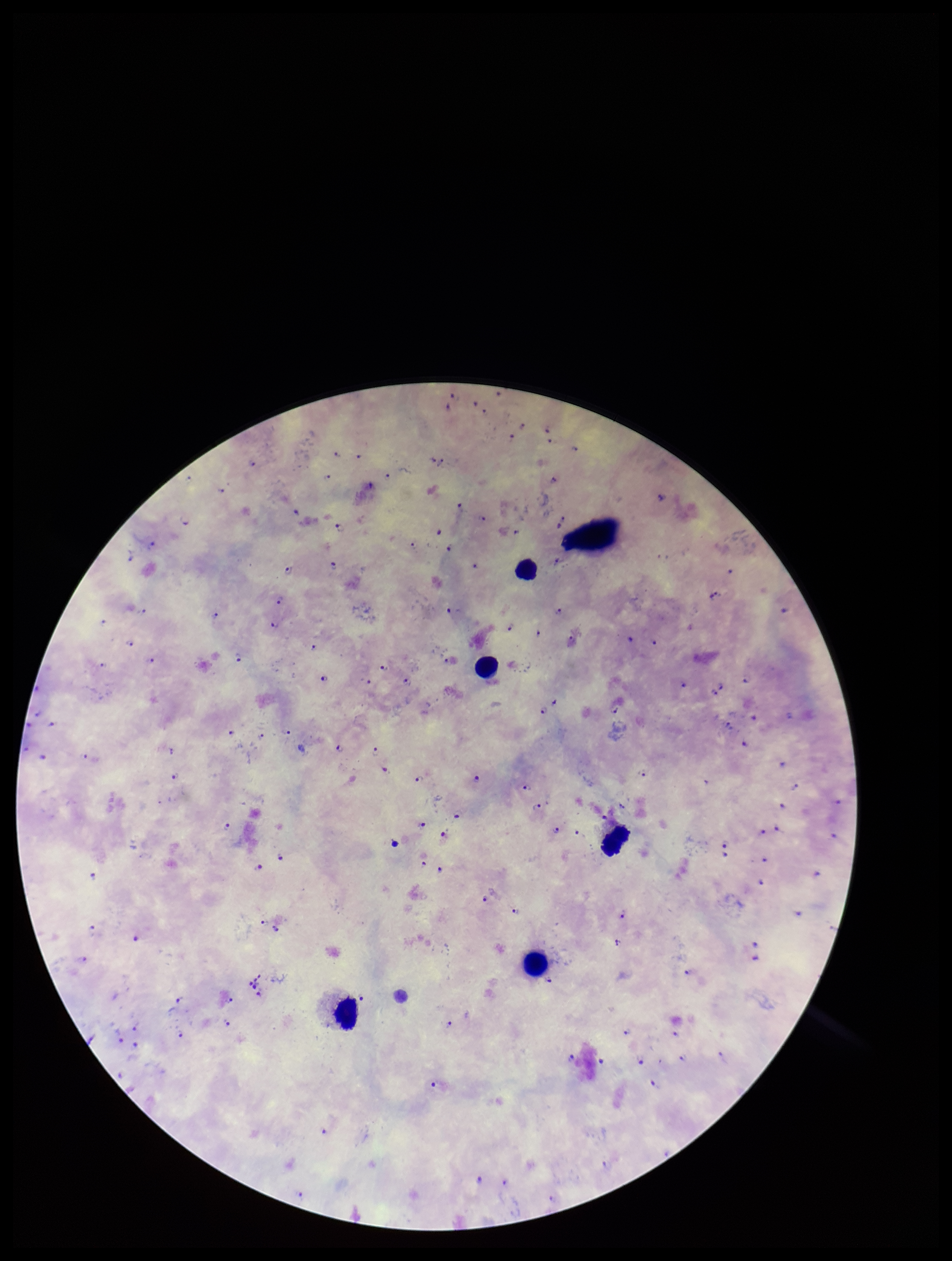
Summary:
  - Field of view: one from this slide
  - Leukocyte count: 5
  - Parasite count: 104
  - Capture: smartphone photograph through the microscope eyepiece
  - Plasmodium parasites: detected
  - Image size: 952×1261 pixels
  - Species reported for this patient: Plasmodium falciparum
  - Patient malaria status: infected
  - Stain: Giemsa
  - Preparation: thick smear